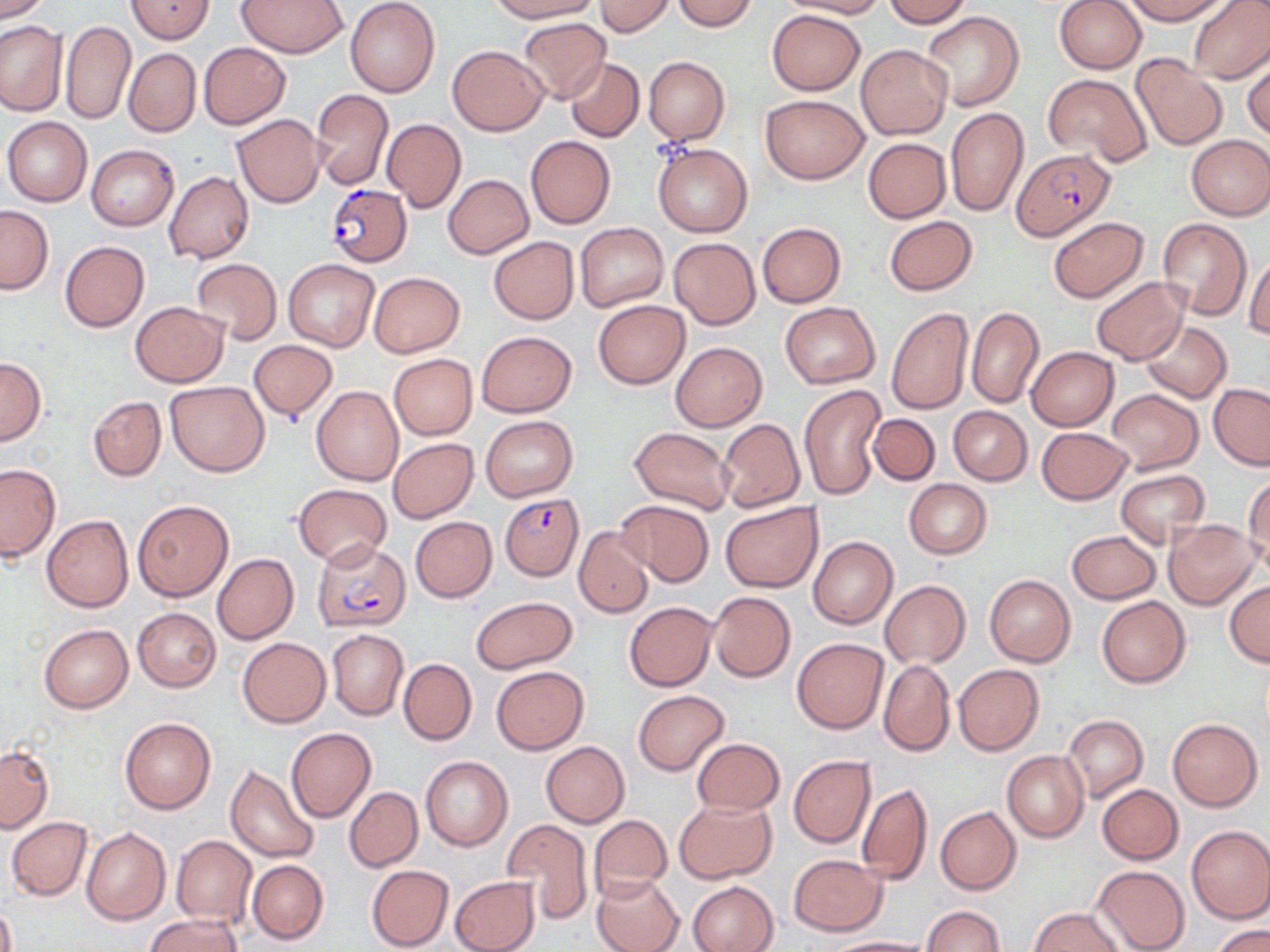
slide-level diagnosis = Plasmodium falciparum
preparation = thin blood smear
modality = light microscopy
Plasmodium falciparum-infected red blood cell locations = approximate bounding boxes as (x1, y1, x2, y2) in pixels: (1013, 149, 1112, 241), (325, 183, 412, 266), (500, 493, 584, 581), (312, 538, 411, 632)
field of view = single
image size = 1270×952 pixels
stain = May-Grünwald-Giemsa
magnification = 1000x
uninfected red blood cell locations = approximate bounding boxes as (x1, y1, x2, y2) in pixels: (0, 0, 52, 22), (126, 0, 214, 44), (238, 0, 348, 57), (345, 0, 441, 98), (489, 0, 601, 22), (596, 0, 673, 37), (672, 0, 758, 31), (780, 0, 888, 18), (882, 0, 970, 26), (1053, 0, 1146, 74), (1125, 0, 1229, 24), (1186, 0, 1270, 83), (766, 9, 865, 95), (922, 10, 1025, 112), (518, 17, 612, 104), (0, 20, 67, 116), (60, 20, 137, 126), (198, 42, 290, 128), (447, 45, 548, 135), (855, 45, 951, 139), (123, 48, 201, 137), (1243, 53, 1270, 140), (643, 55, 729, 146), (1131, 55, 1229, 150), (565, 58, 645, 143), (1043, 73, 1151, 168), (311, 88, 393, 189), (759, 93, 869, 183), (945, 106, 1028, 217), (232, 114, 324, 209), (3, 116, 92, 206), (381, 118, 465, 212), (1185, 134, 1270, 220), (526, 135, 616, 229), (862, 138, 951, 223), (653, 142, 752, 237), (86, 145, 178, 230), (165, 171, 254, 265), (443, 174, 533, 259), (0, 205, 53, 293), (883, 216, 977, 294), (1048, 216, 1149, 303), (1156, 218, 1252, 319), (756, 222, 846, 308), (575, 223, 668, 311), (487, 236, 580, 325), (668, 237, 761, 329), (59, 241, 150, 332), (1244, 252, 1270, 339), (192, 258, 282, 344), (283, 259, 379, 351), (370, 272, 465, 357), (1090, 277, 1189, 365), (592, 300, 689, 388), (130, 301, 228, 387), (780, 302, 880, 388), (966, 306, 1044, 409), (885, 307, 974, 413), (1141, 322, 1231, 402), (476, 331, 577, 417), (248, 340, 336, 421), (670, 341, 766, 431), (1026, 346, 1119, 431), (389, 354, 477, 439), (0, 357, 46, 446), (165, 381, 269, 477), (1208, 383, 1270, 469), (799, 384, 885, 501), (311, 386, 404, 486), (1105, 389, 1203, 473), (88, 395, 165, 482), (947, 406, 1031, 486), (869, 413, 940, 485), (481, 415, 577, 500), (718, 418, 804, 512), (629, 427, 735, 513), (1036, 427, 1135, 504), (388, 437, 478, 523), (1, 464, 60, 560), (1114, 469, 1210, 547), (1243, 474, 1270, 572), (904, 479, 991, 558), (294, 484, 392, 566), (133, 499, 233, 601), (616, 500, 713, 585), (718, 500, 822, 593), (42, 515, 134, 612), (410, 517, 497, 601), (1164, 519, 1261, 609), (574, 526, 653, 617), (1066, 531, 1160, 604), (808, 536, 898, 629), (213, 554, 298, 645), (985, 574, 1075, 666), (880, 580, 970, 669), (1225, 581, 1270, 666), (708, 592, 795, 682), (1097, 595, 1191, 688), (471, 596, 578, 673), (624, 601, 716, 691), (133, 607, 221, 691), (40, 624, 133, 713), (327, 629, 408, 721), (238, 637, 330, 727), (792, 637, 888, 733), (399, 658, 477, 745), (878, 659, 955, 757), (952, 664, 1045, 756), (492, 665, 588, 753), (634, 689, 729, 774), (1062, 715, 1148, 803), (120, 717, 216, 814), (1168, 718, 1262, 812), (286, 727, 376, 823), (690, 738, 784, 814), (541, 741, 628, 827), (0, 746, 53, 833), (1002, 750, 1089, 843), (420, 755, 513, 852), (788, 755, 875, 846), (225, 765, 320, 863), (857, 781, 933, 885), (1097, 784, 1183, 864), (344, 786, 423, 872), (675, 799, 777, 883), (935, 807, 1022, 895), (589, 813, 673, 900), (6, 817, 92, 900), (501, 819, 593, 924), (1186, 826, 1270, 924), (81, 827, 170, 925), (171, 835, 257, 927), (788, 854, 887, 935), (247, 859, 329, 944), (366, 865, 454, 951), (1090, 865, 1190, 952), (592, 873, 684, 952), (449, 876, 539, 952), (689, 881, 777, 952), (0, 900, 16, 952), (920, 905, 1005, 952), (1029, 907, 1124, 951), (146, 914, 242, 952), (1212, 925, 1270, 952), (820, 937, 937, 952)